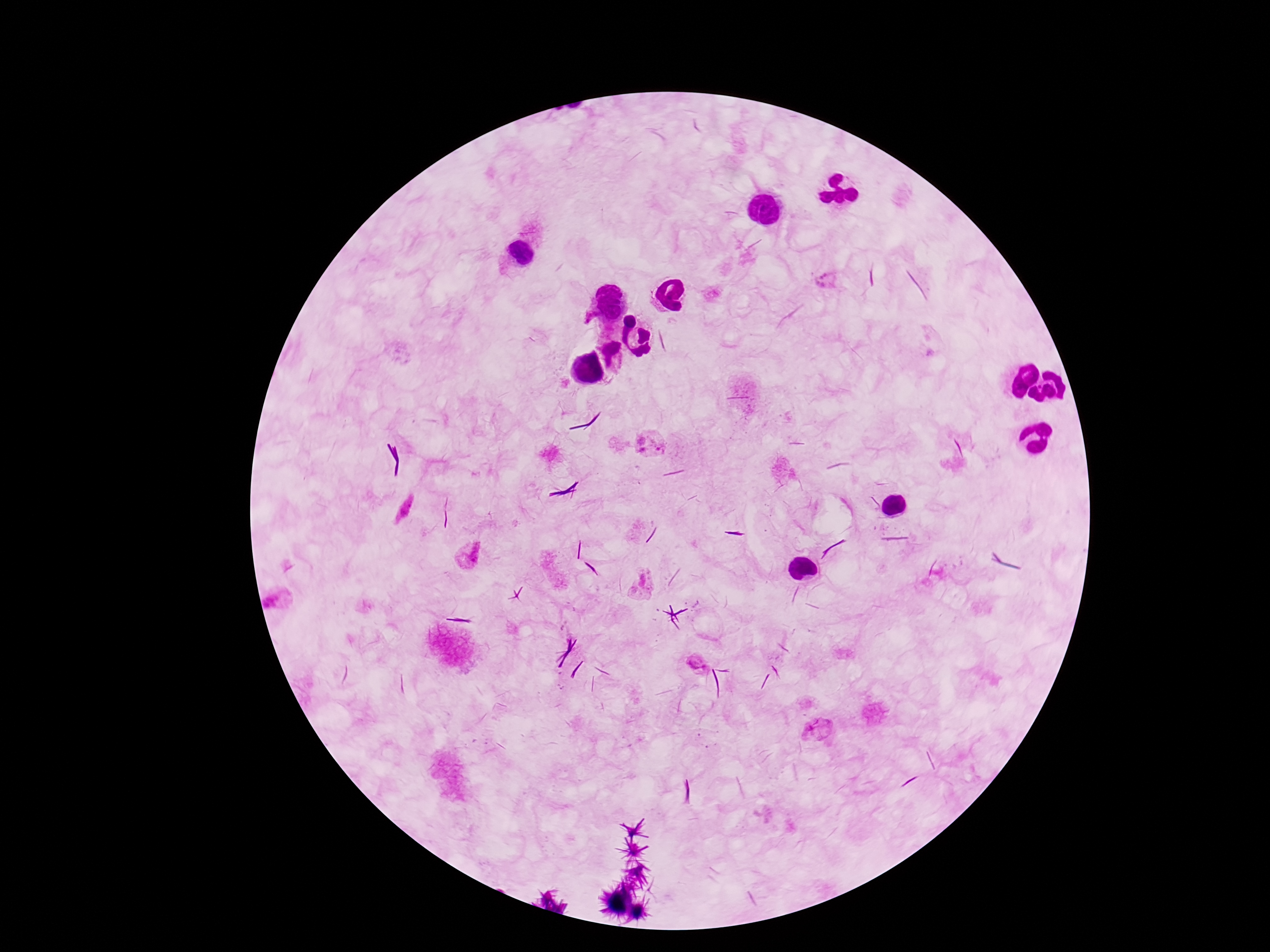
capture: smartphone camera through the microscope eyepiece
magnification: 100x
plasmodium_parasite_locations: 'approximate object centers, in pixels from the top-left corner: (x=826, y=281), (x=650, y=446), (x=404, y=509), (x=468, y=554), (x=644, y=585), (x=277, y=604), (x=696, y=664), (x=817, y=730)'
stain: Giemsa
field_of_view: one from this slide
preparation: thick blood smear
image_size: 1270×952 pixels
patient_malaria_status: infected